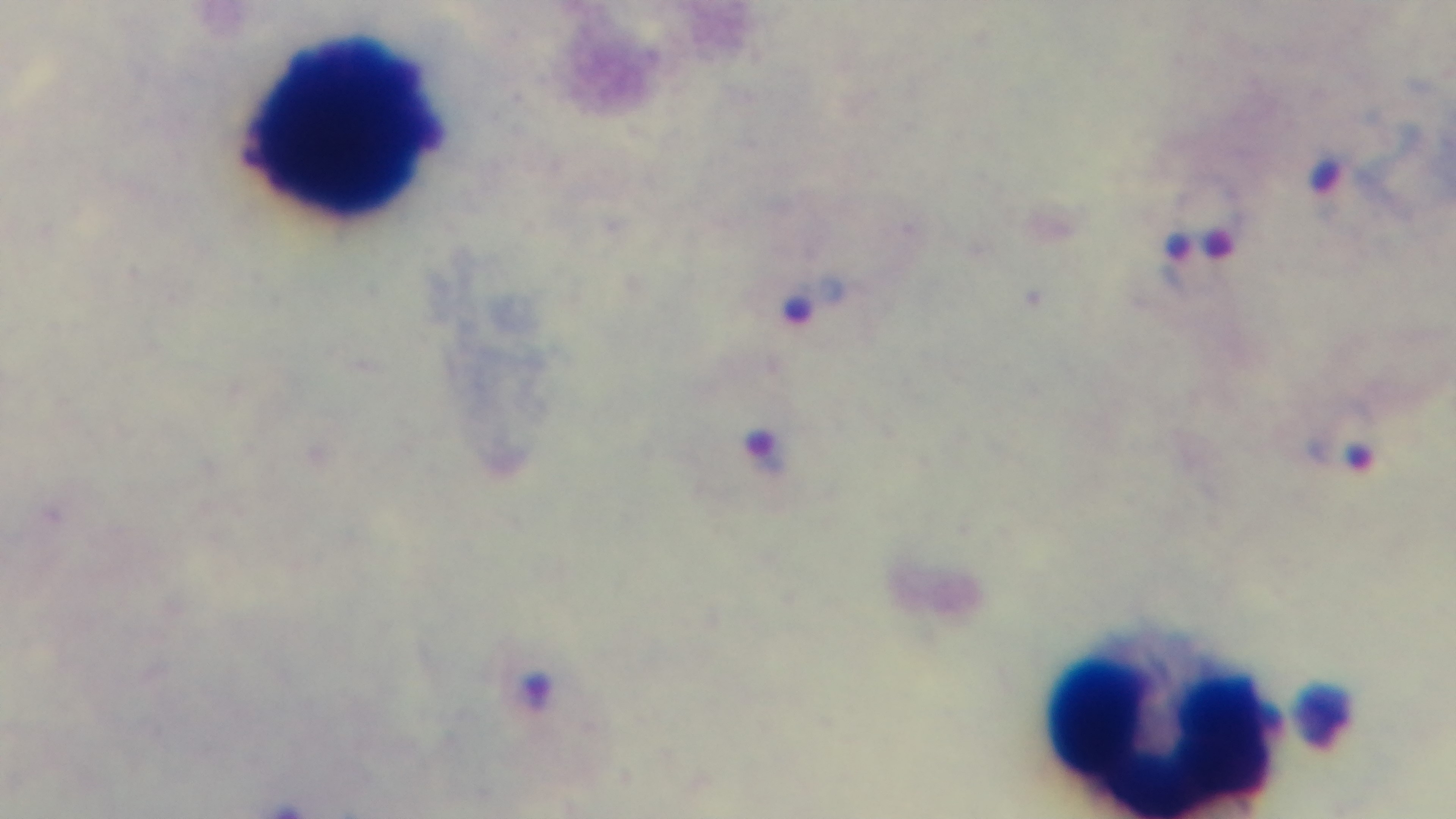
Summary:
  - Field of view: one from the slide
  - Preparation: thick
  - Objective: 100x oil immersion
  - Stain: Giemsa
  - Capture: mounted 4K digital camera
  - Modality: light microscopy
  - Malaria status: infected